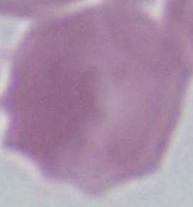
Photomicrograph. 1000x magnification. An erythrocyte is seen.